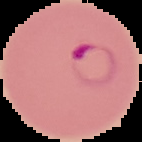
image type = cell region segmented out of the field of view; surrounding area masked to black
image size = 142×142 pixels
result = malaria parasites identified
preparation = thin blood film